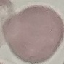
malaria status = uninfected
image type = cell patch, automatically extracted from a larger field of view and resized to 64 × 64 pixels
stain = Giemsa
capture = smartphone through the microscope eyepiece
preparation = thin smear